Assess for malaria.
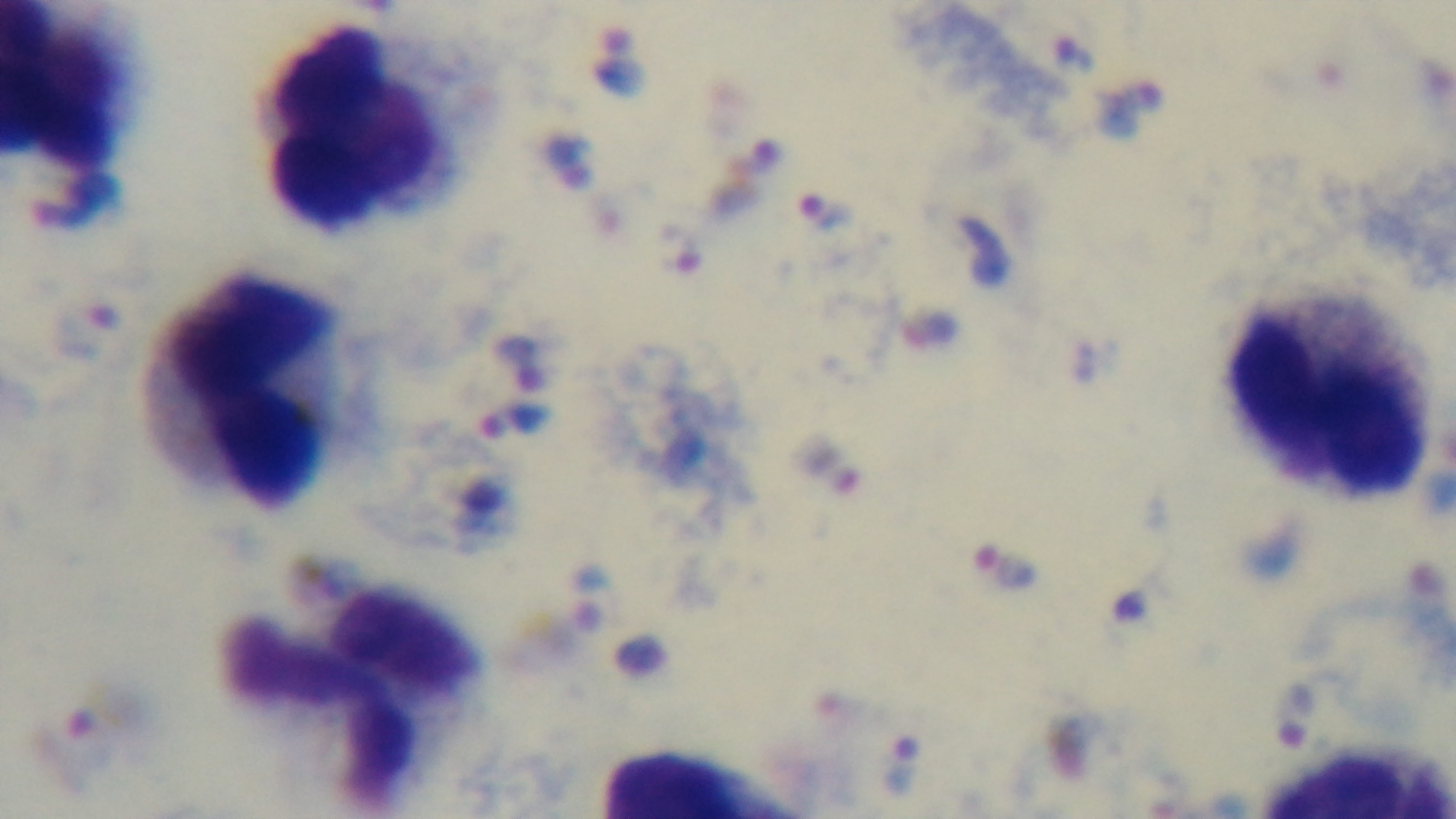
It is infected.

Captured with a mounted 4K digital camera. One field from the slide. Light microscopy. 100x oil-immersion objective. Preparation: thick. Giemsa-stained.